Locate and identify every blood parasite.
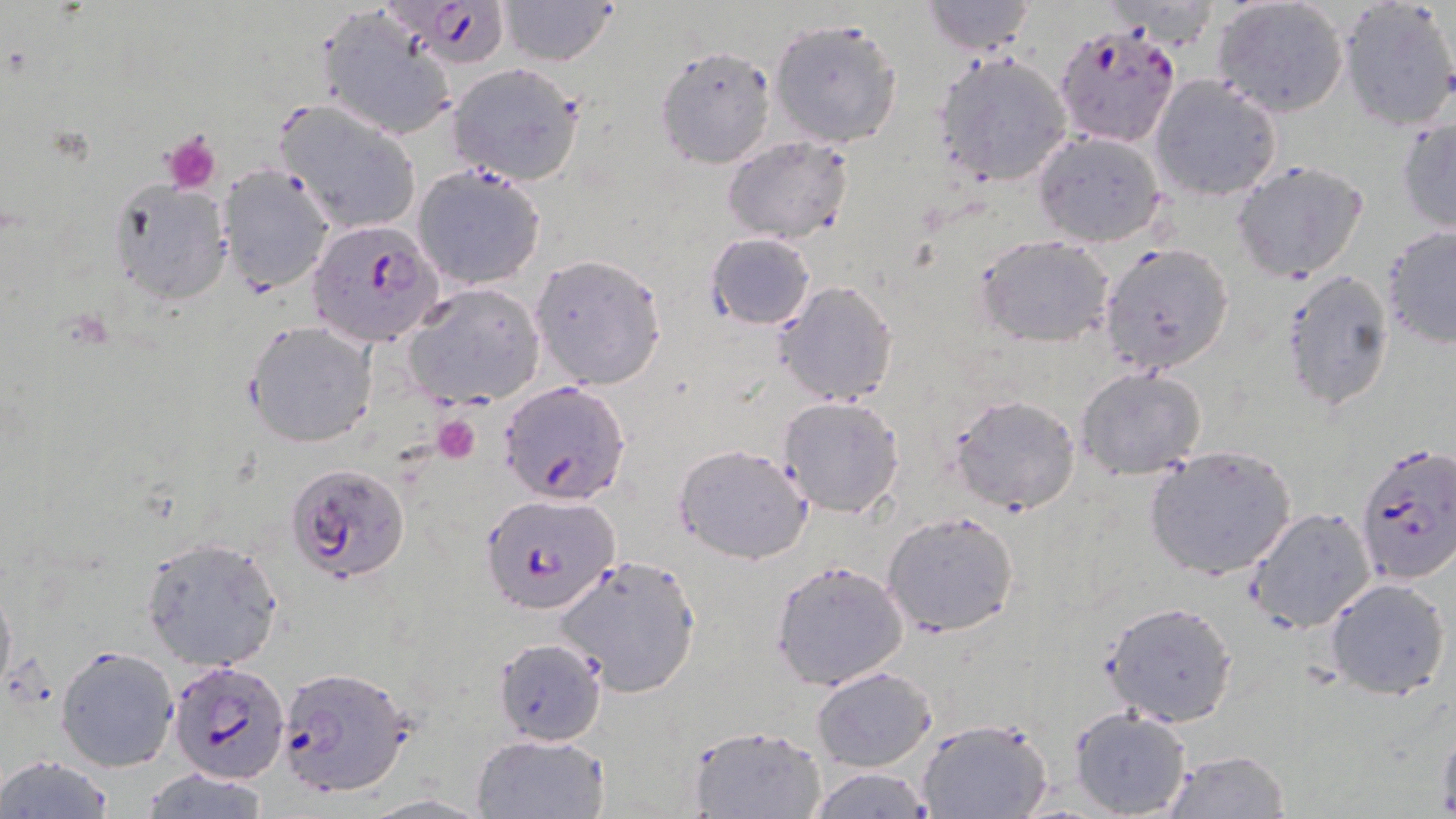
Approximate bounding boxes as (x1, y1, x2, y2) in pixels.
Plasmodium falciparum-infected red blood cells: (382, 2, 511, 72), (1053, 22, 1181, 148), (306, 221, 443, 347), (500, 380, 630, 503), (1355, 444, 1456, 582), (290, 464, 412, 585), (481, 489, 619, 615), (169, 659, 288, 783), (279, 666, 414, 796).
No Plasmodium ovale, Plasmodium malariae, Plasmodium vivax, Babesia divergens, or Trypanosoma brucei observed.

Uninfected red blood cell locations: (496, 0, 619, 67), (1211, 0, 1350, 118), (920, 1, 1039, 55), (1338, 1, 1456, 132), (315, 7, 457, 141), (768, 16, 905, 148), (653, 45, 777, 169), (933, 51, 1074, 187), (446, 63, 587, 186), (1149, 75, 1282, 201), (275, 100, 421, 235), (1397, 116, 1456, 234), (1031, 130, 1167, 247), (722, 135, 854, 244), (1231, 160, 1369, 283), (217, 164, 335, 293), (412, 164, 546, 291), (107, 179, 231, 304), (1380, 226, 1456, 349), (706, 232, 815, 330), (975, 235, 1114, 346), (1098, 242, 1234, 377), (530, 254, 668, 389), (1279, 269, 1396, 411), (773, 280, 898, 405), (405, 284, 545, 408), (246, 321, 377, 447), (1076, 366, 1206, 480), (948, 393, 1081, 515), (777, 395, 906, 517), (674, 443, 814, 563), (1144, 443, 1300, 581), (1246, 506, 1377, 633), (884, 510, 1021, 637), (138, 535, 283, 671), (552, 553, 703, 698), (770, 559, 907, 690), (1324, 576, 1451, 699), (0, 580, 15, 702), (1101, 601, 1237, 726), (493, 637, 609, 746), (55, 645, 180, 772), (811, 666, 937, 771), (1069, 706, 1192, 818), (916, 717, 1054, 819), (686, 723, 828, 819), (1436, 723, 1456, 815), (470, 732, 609, 818), (1163, 750, 1291, 818), (0, 756, 114, 819), (137, 765, 271, 818), (807, 767, 932, 819). Platelet locations: (160, 130, 223, 194), (434, 415, 481, 464). Slide-level diagnosis: Plasmodium falciparum. Light microscopy. Thin blood film. 1000x magnification. May-Grünwald-Giemsa stain. Image is 1456×819 pixels. One field of a larger specimen.